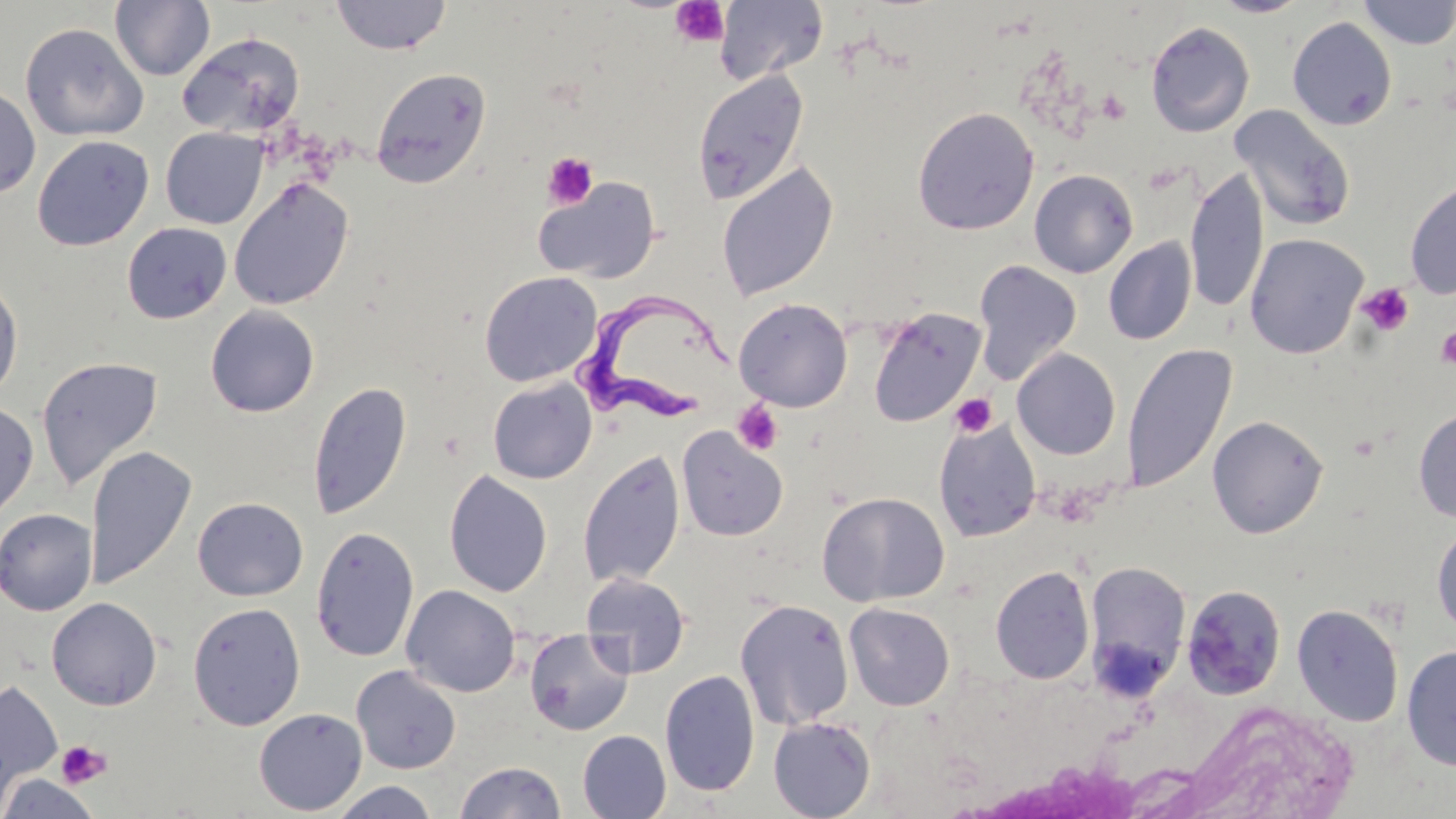

slide_level_diagnosis: Trypanosoma brucei
stain: May-Grünwald-Giemsa
platelet_locations: 'approximate bounding boxes as (x1, y1, x2, y2) in pixels: (671, 1, 730, 48), (542, 152, 599, 209), (1356, 283, 1414, 337), (1436, 327, 1456, 370), (949, 394, 997, 438), (732, 400, 784, 455), (55, 740, 111, 789)'
preparation: thin blood smear
image_size: 1456×819 pixels
trypanosoma_brucei_locations: 'approximate bounding boxes as (x1, y1, x2, y2) in pixels: (574, 282, 737, 423)'
field_of_view: single
uninfected_red_blood_cell_locations: 'approximate bounding boxes as (x1, y1, x2, y2) in pixels: (330, 0, 452, 55), (1210, 0, 1310, 18), (1359, 0, 1456, 49), (110, 1, 215, 81), (714, 1, 829, 86), (1287, 17, 1397, 131), (1145, 22, 1255, 137), (20, 23, 148, 141), (178, 32, 305, 137), (370, 68, 491, 189), (692, 69, 809, 206), (0, 83, 40, 200), (1229, 105, 1355, 232), (913, 107, 1039, 235), (160, 127, 267, 229), (32, 134, 154, 251), (716, 161, 838, 302), (1185, 166, 1269, 315), (1029, 169, 1138, 278), (534, 176, 661, 285), (229, 177, 354, 310), (1404, 179, 1456, 300), (121, 222, 232, 324), (1245, 233, 1368, 359), (1103, 237, 1197, 346), (972, 260, 1083, 385), (479, 271, 602, 387), (0, 273, 24, 403), (734, 298, 853, 412), (205, 304, 320, 417), (867, 307, 986, 427), (1121, 342, 1236, 495), (1012, 347, 1121, 460), (36, 356, 163, 492), (487, 378, 597, 484), (307, 379, 412, 520), (0, 402, 39, 523), (1413, 407, 1456, 523), (1207, 415, 1329, 538), (934, 417, 1042, 542), (677, 427, 788, 542), (84, 444, 197, 591), (578, 449, 686, 589), (443, 470, 553, 598), (817, 491, 950, 606), (192, 497, 308, 601), (0, 508, 98, 616), (1432, 522, 1456, 637), (310, 525, 420, 662), (1083, 561, 1191, 696), (990, 564, 1095, 685), (580, 572, 690, 678), (1181, 584, 1286, 700), (400, 585, 521, 697), (46, 597, 162, 710), (734, 598, 854, 730), (188, 602, 306, 730), (844, 603, 955, 711), (1292, 603, 1404, 727), (524, 629, 635, 736), (1401, 643, 1456, 771), (350, 665, 462, 775), (660, 669, 760, 797), (0, 681, 63, 802), (1175, 702, 1363, 819), (253, 707, 368, 815), (767, 716, 876, 818), (578, 730, 671, 818), (453, 760, 567, 819), (0, 773, 101, 819), (328, 781, 440, 819)'
modality: optical microscopy
magnification: 1000x